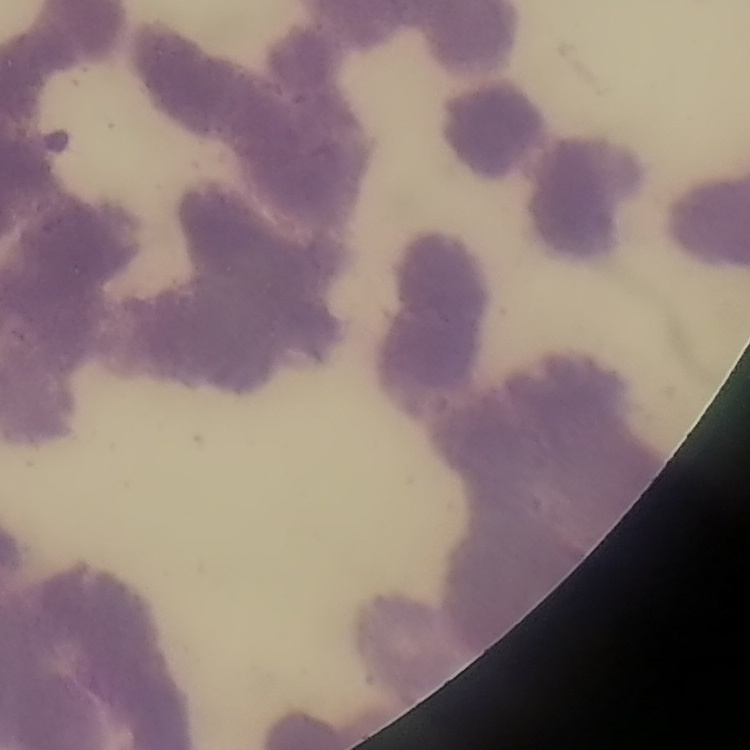

erythrocyte_morphology: rouleaux formation
preparation: thin peripheral smear
image_type: one tile cut from a larger photomicrograph
stain: Field's or Giemsa